Outline platelets.
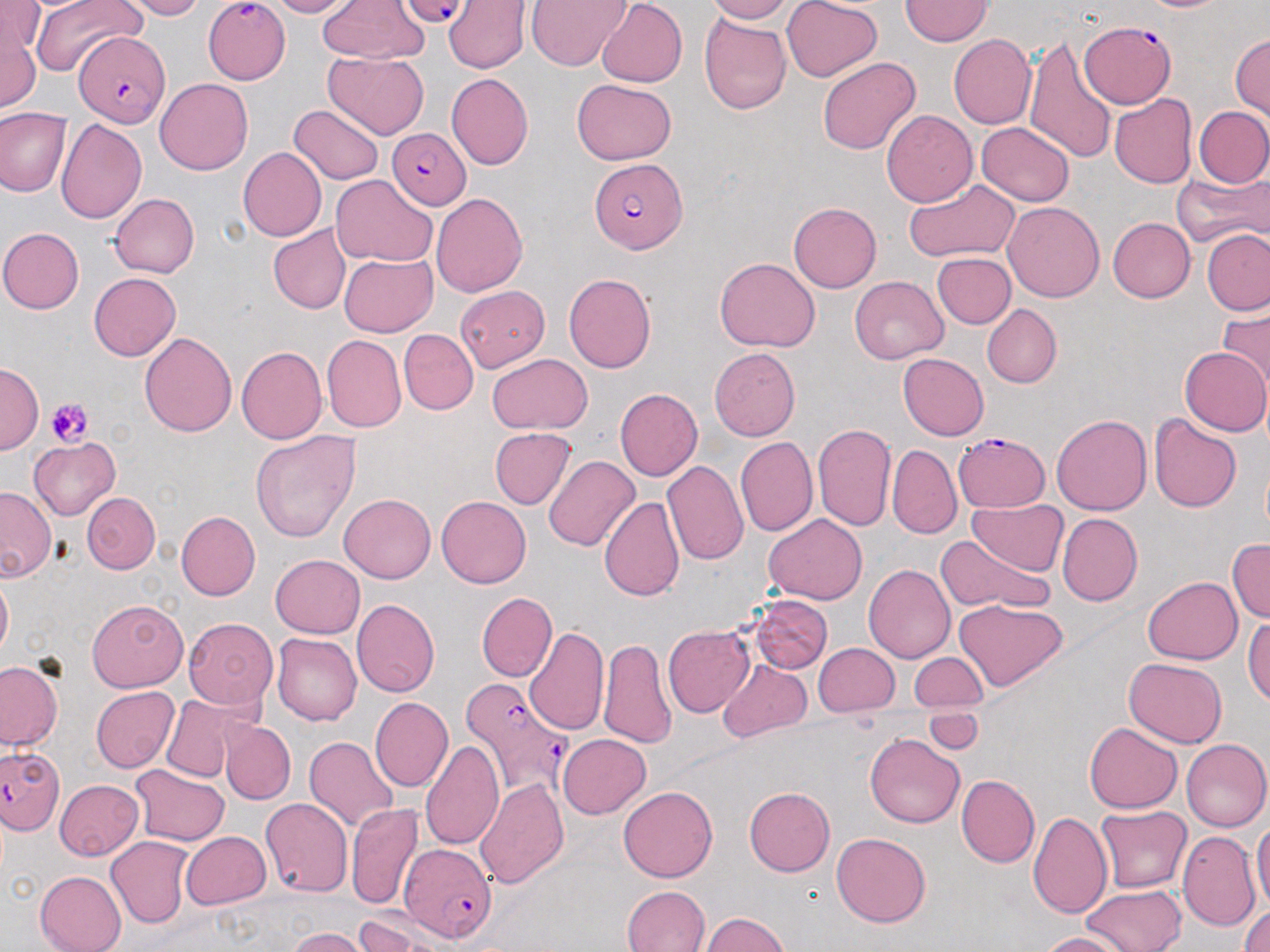
Approximate bounding boxes as (x1,y1)-(x2,y2) corner pairs in pixels.
Platelets: (46,397)-(93,448).

Uninfected red blood cell locations: (30,0)-(142,77), (120,0)-(204,20), (267,0)-(354,18), (704,0)-(793,24), (782,0)-(881,82), (900,0)-(993,46), (318,1)-(429,63), (443,1)-(530,73), (527,1)-(632,71), (596,1)-(687,87), (0,3)-(43,61), (699,13)-(791,114), (1,15)-(41,113), (1231,33)-(1270,121), (948,34)-(1035,130), (1023,35)-(1117,164), (323,52)-(429,139), (817,56)-(920,155), (447,73)-(534,170), (155,78)-(252,174), (571,78)-(677,165), (1109,93)-(1196,188), (289,105)-(383,184), (1194,106)-(1270,187), (0,108)-(72,198), (881,109)-(978,207), (55,119)-(146,222), (976,122)-(1075,207), (238,147)-(327,241), (1172,169)-(1270,249), (330,174)-(438,265), (904,178)-(1020,260), (431,193)-(528,297), (110,194)-(200,278), (1003,201)-(1105,302), (789,202)-(881,293), (1107,217)-(1196,302), (268,223)-(351,314), (0,228)-(84,314), (1203,229)-(1270,316), (932,252)-(1015,329), (338,253)-(436,337), (715,257)-(820,352), (88,272)-(180,361), (563,272)-(656,373), (849,276)-(949,364), (456,285)-(550,373), (981,304)-(1061,387), (1219,308)-(1270,392), (399,329)-(478,415), (139,331)-(237,437), (321,334)-(406,432), (236,346)-(326,443), (1179,346)-(1270,437), (709,347)-(801,441), (898,352)-(989,440), (486,353)-(593,434), (0,361)-(42,454), (614,388)-(703,480), (1052,413)-(1152,515), (1149,415)-(1242,514), (812,424)-(895,532), (488,428)-(577,509), (251,431)-(362,544), (735,436)-(818,537), (29,437)-(121,519), (886,444)-(961,540), (544,455)-(640,551), (662,461)-(748,565), (0,486)-(56,581), (82,493)-(160,574), (338,493)-(436,583), (437,496)-(531,588), (598,496)-(683,601), (969,499)-(1068,576), (176,510)-(260,600), (1057,513)-(1142,606), (764,514)-(867,605), (936,534)-(1053,616), (1228,537)-(1269,623), (270,555)-(365,639), (863,565)-(955,663), (0,570)-(12,663), (1144,577)-(1242,664), (477,592)-(557,682), (748,594)-(832,675), (351,598)-(440,697), (87,599)-(188,692), (954,599)-(1068,692), (182,617)-(279,709), (1244,617)-(1270,704), (662,625)-(754,718), (525,626)-(610,737), (272,632)-(362,725), (599,637)-(677,749), (814,643)-(899,716), (909,651)-(988,711), (1123,657)-(1228,747), (718,658)-(811,741), (0,659)-(63,751), (91,686)-(179,772), (161,694)-(256,782), (370,698)-(452,791), (925,708)-(985,756), (221,721)-(294,803), (1084,722)-(1182,813), (865,733)-(965,828), (557,734)-(651,818), (305,736)-(399,832), (1181,739)-(1270,832), (421,740)-(504,852), (130,764)-(229,847), (956,775)-(1039,867), (473,777)-(568,889), (54,779)-(144,861), (619,786)-(718,882), (744,786)-(835,876), (259,799)-(353,898), (345,803)-(423,910), (1096,806)-(1192,893), (1029,811)-(1112,919), (1251,820)-(1270,914), (181,830)-(271,909), (1177,831)-(1261,932), (831,832)-(931,927), (107,836)-(193,928), (35,871)-(127,952), (1082,884)-(1186,951), (622,885)-(710,952), (1239,903)-(1270,952), (353,911)-(442,952), (697,912)-(791,951), (287,927)-(369,952), (1038,931)-(1133,952). Plasmodium falciparum-infected red blood cell locations: (399,1)-(472,29), (204,2)-(290,84), (1079,20)-(1176,107), (73,32)-(170,129), (386,127)-(470,209), (589,158)-(685,255), (952,432)-(1050,513), (460,679)-(571,800), (0,745)-(63,833), (398,845)-(497,944). Slide-level diagnosis: Plasmodium falciparum. Optical microscopy. 1000x magnification. May-Grünwald-Giemsa-stained preparation. Image is 1270×952 pixels. Single field of view. Thin blood film.